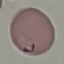

Summary:
  - Result: malaria parasites detected
  - Preparation: thin blood smear
  - Capture: smartphone through the microscope eyepiece
  - Stain: Giemsa
  - Image type: cell patch, automatically extracted from a larger field of view and resized to 64 × 64 pixels